Assess this cell for malaria.
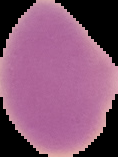

It is uninfected.

Summary:
  - Preparation: thin blood smear
  - Image type: segmented cell region on a black background
  - Image size: 118×157 pixels